Assess this cell for malaria.
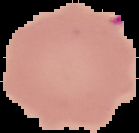

It is uninfected.

image size = 139×133 pixels
preparation = thin blood smear
image type = cell region segmented out of the field of view; surrounding area masked to black